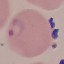

result = malaria parasites identified
image type = cell patch, automatically extracted from a larger field of view and resized to 64 × 64 pixels
stain = Giemsa
capture = smartphone camera at the microscope eyepiece
preparation = thin blood smear